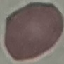

Summary:
  - Result: no malaria parasites detected
  - Capture: smartphone camera at the microscope eyepiece
  - Stain: Giemsa
  - Preparation: thin blood smear
  - Image type: cell patch, automatically extracted from a larger field of view and resized to 64 × 64 pixels